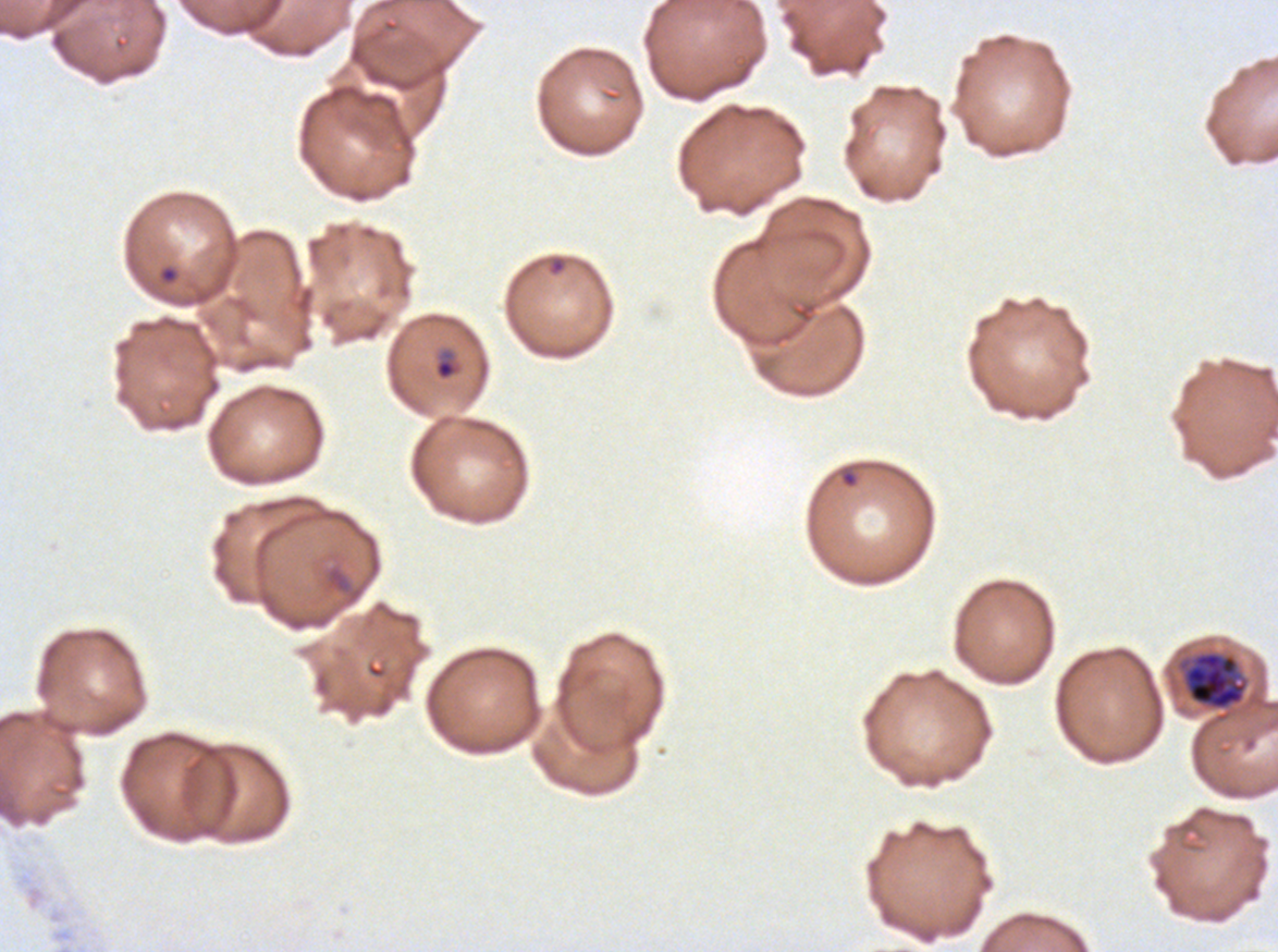

Approximate bounding boxes as [x1, y1, x2, y2] in pixels.
Summary:
  - Early schizont locations: [1183, 651, 1247, 710]
  - Debris locations: [325, 563, 364, 605]
  - Late-ring/early-trophozoite locations: [433, 348, 463, 382]
  - Ring locations: [159, 266, 178, 284]
  - Life-cycle stages observed: ring, late-ring/early-trophozoite, early schizont
  - Image size: 1278×952 pixels
  - Specimen: ex-vivo Plasmodium falciparum culture from a patient in The Gambia, grown for 24 to 48 hours
  - Stain: Giemsa
  - Preparation: thin blood film
  - Field of view: one sub-image of a larger composite